Assess this cell for malaria.
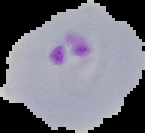
It is parasitized.

Segmented cell region on a black background. From a thin blood smear. Image is 145×133 pixels.